State which parasite is depicted.
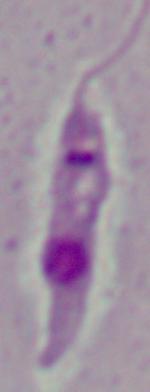
Leishmania.

{
  "modality": "micrograph",
  "magnification": "1000x"
}